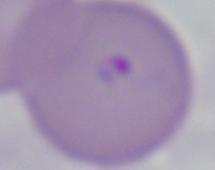
Captured at 1000x magnification. Micrograph. A Babesia parasite is seen.